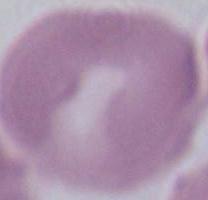

{
  "modality": "photomicrograph",
  "identification": "red blood cell",
  "magnification": "1000x"
}